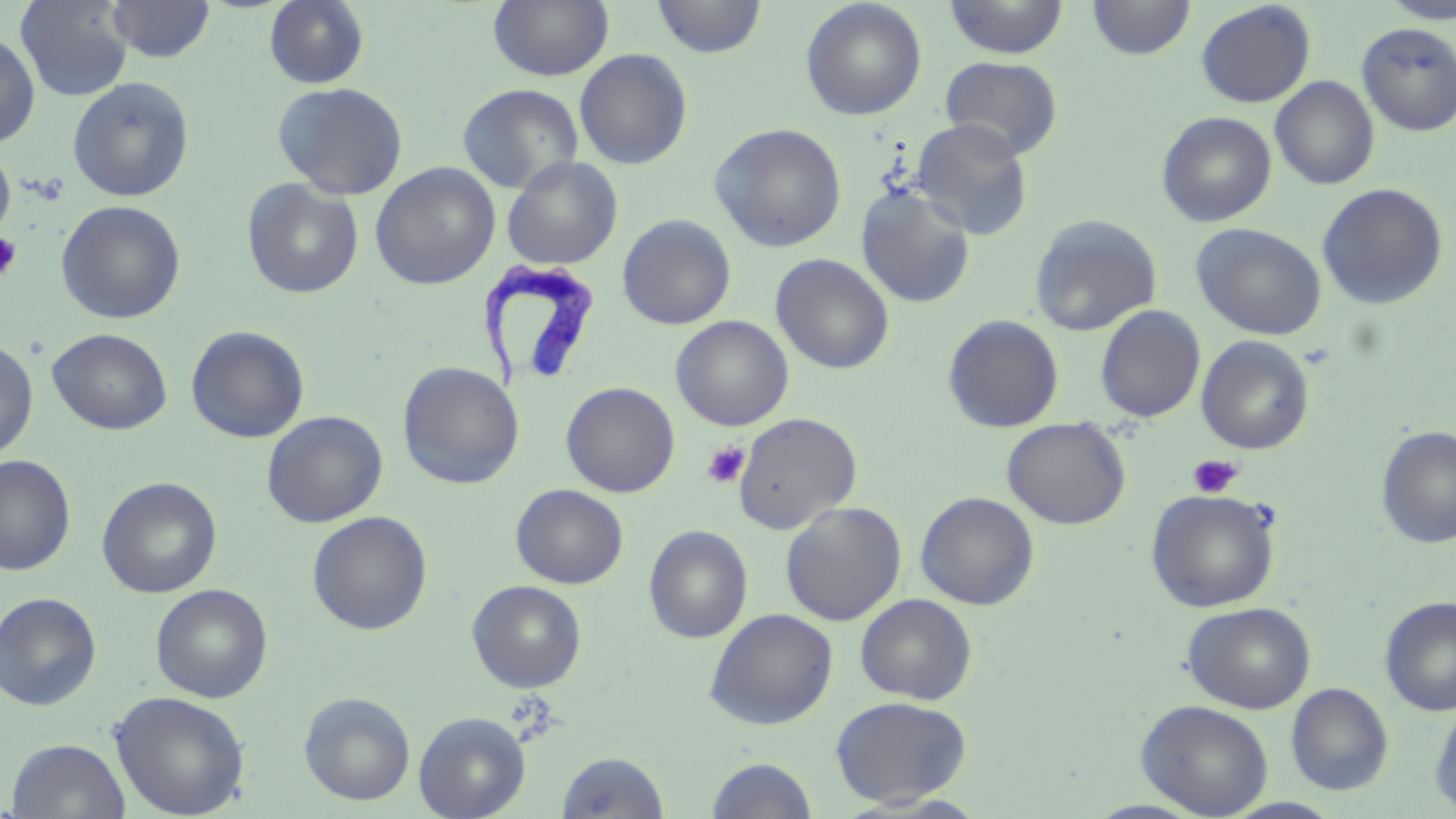

Summary:
  - Coordinate format: approximate bounding boxes as (x1,y1)-(x2,y2) corner pairs in pixels
  - Trypanosoma brucei locations: (478,261)-(602,392)
  - Platelet locations: (0,231)-(23,281), (701,441)-(750,488), (1188,455)-(1242,498)
  - Uninfected red blood cell locations: (15,0)-(135,101), (108,0)-(216,63), (488,0)-(614,81), (651,0)-(768,59), (1087,0)-(1196,60), (1379,0)-(1456,24), (263,1)-(370,89), (800,1)-(927,121), (943,1)-(1069,59), (1195,1)-(1316,108), (1357,22)-(1456,136), (0,30)-(40,148), (574,48)-(693,170), (939,55)-(1063,160), (1270,75)-(1380,190), (67,76)-(195,202), (272,82)-(409,200), (457,83)-(584,194), (1157,111)-(1277,227), (910,118)-(1033,240), (710,122)-(847,252), (0,142)-(15,240), (502,156)-(623,270), (370,162)-(500,290), (241,178)-(364,299), (1317,182)-(1449,309), (856,186)-(976,309), (56,199)-(186,324), (617,214)-(736,330), (1028,214)-(1162,337), (1191,223)-(1326,340), (771,253)-(895,374), (1095,305)-(1206,423), (943,314)-(1064,433), (671,315)-(793,431), (186,325)-(310,444), (47,328)-(172,435), (1196,335)-(1315,454), (0,338)-(38,460), (397,361)-(524,489), (561,381)-(680,498), (262,411)-(387,527), (733,412)-(862,534), (1002,417)-(1131,530), (1375,425)-(1456,548), (1,454)-(76,576), (97,476)-(222,597), (511,484)-(628,588), (1145,488)-(1282,612), (915,491)-(1040,610), (780,501)-(907,626), (308,511)-(433,635), (644,524)-(753,643), (467,580)-(587,693), (151,584)-(273,703), (0,591)-(102,710), (855,593)-(978,704), (1380,596)-(1456,717), (1183,601)-(1316,713), (705,608)-(839,730), (1286,682)-(1394,796), (110,691)-(250,818), (299,692)-(416,806), (830,695)-(972,807), (1136,699)-(1274,817), (1428,701)-(1456,815), (413,710)-(531,819), (5,738)-(131,818), (558,750)-(671,818), (706,756)-(818,818)
  - Slide-level diagnosis: Trypanosoma brucei
  - Preparation: thin blood smear
  - Modality: optical microscopy
  - Image size: 1456×819 pixels
  - Stain: May-Grünwald-Giemsa
  - Magnification: 1000x
  - Field of view: one of a larger specimen